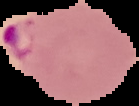 Image is 139×106 pixels. Cell region segmented out of the field of view; the surrounding area is masked to black. From a thin blood film. Malaria status: parasitized.